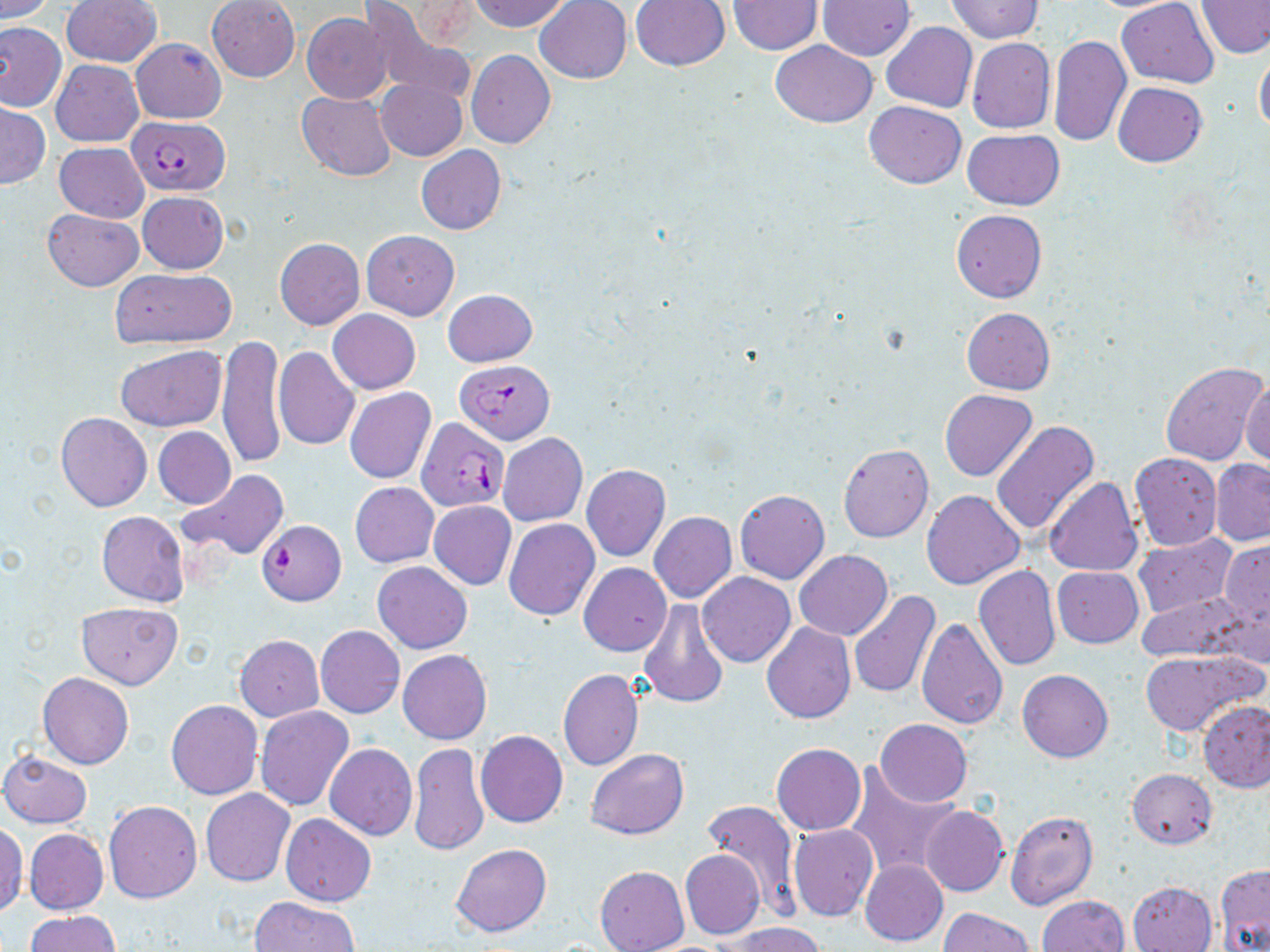 Approximate bounding boxes as [x1, y1, x2, y2] in pixels. Uninfected red blood cell locations: [1, 0, 55, 22], [61, 0, 161, 67], [356, 0, 475, 105], [470, 0, 571, 33], [534, 0, 632, 84], [728, 0, 823, 54], [818, 0, 914, 60], [949, 0, 1042, 42], [1117, 0, 1220, 87], [1197, 0, 1270, 59], [207, 1, 299, 82], [629, 1, 731, 72], [302, 14, 390, 103], [0, 21, 66, 112], [880, 22, 978, 113], [1047, 33, 1131, 147], [132, 37, 225, 123], [966, 37, 1056, 134], [769, 40, 877, 127], [1254, 46, 1270, 139], [466, 50, 556, 149], [52, 59, 144, 147], [376, 78, 468, 162], [1113, 82, 1207, 166], [297, 91, 395, 181], [864, 101, 967, 188], [1, 103, 50, 188], [961, 129, 1065, 210], [54, 141, 148, 222], [416, 145, 506, 235], [137, 191, 228, 274], [42, 209, 143, 291], [951, 209, 1047, 302], [362, 230, 459, 320], [275, 238, 365, 329], [109, 268, 236, 349], [443, 289, 537, 367], [962, 307, 1055, 394], [328, 309, 421, 394], [218, 335, 285, 469], [115, 344, 225, 432], [272, 346, 360, 451], [1160, 362, 1269, 467], [1242, 373, 1270, 470], [345, 387, 436, 483], [940, 389, 1037, 482], [55, 412, 152, 512], [990, 420, 1100, 536], [153, 426, 235, 509], [498, 433, 587, 527], [837, 444, 933, 543], [1129, 453, 1222, 551], [1210, 458, 1270, 545], [582, 464, 670, 561], [177, 469, 287, 561], [1043, 478, 1143, 577], [350, 482, 438, 567], [735, 490, 829, 584], [921, 490, 1025, 589], [428, 500, 516, 590], [97, 511, 189, 606], [649, 512, 737, 603], [504, 518, 598, 620], [1133, 532, 1237, 618], [1219, 540, 1269, 627], [794, 550, 893, 640], [373, 562, 472, 653], [579, 563, 671, 656], [973, 565, 1062, 670], [1052, 566, 1143, 647], [698, 572, 795, 667], [847, 590, 941, 700], [1136, 591, 1256, 663], [638, 600, 728, 710], [76, 601, 183, 689], [763, 603, 938, 709], [916, 617, 1007, 730], [761, 622, 856, 723], [315, 625, 404, 717], [235, 635, 323, 721], [397, 649, 492, 744], [1138, 650, 1261, 737], [557, 668, 643, 770], [1017, 669, 1112, 762], [38, 672, 133, 769], [166, 700, 263, 800], [1199, 700, 1270, 792], [256, 706, 353, 811], [874, 719, 971, 807], [476, 730, 568, 827], [324, 743, 417, 840], [409, 743, 488, 856], [771, 743, 866, 835], [585, 749, 689, 839], [1, 751, 91, 827], [848, 768, 961, 881], [1128, 768, 1216, 849], [201, 789, 295, 887], [104, 800, 202, 903], [701, 801, 802, 914], [920, 806, 1008, 897], [1004, 808, 1098, 911], [280, 814, 376, 907], [0, 822, 26, 917], [789, 824, 878, 921], [24, 829, 108, 914], [452, 844, 551, 937], [680, 850, 765, 939], [860, 859, 947, 947], [1215, 865, 1270, 951], [595, 866, 688, 952], [1126, 880, 1217, 952], [1037, 895, 1129, 952], [250, 897, 360, 952], [940, 909, 1033, 952], [25, 910, 122, 952], [726, 923, 823, 952]. Plasmodium falciparum-infected red blood cell locations: [127, 115, 230, 196], [455, 358, 557, 442], [417, 416, 507, 512], [257, 519, 345, 606]. Slide-level diagnosis: Plasmodium falciparum. Thin blood smear. May-Grünwald-Giemsa stain. 1000x magnification. Optical microscopy. Single field of view. Image is 1270×952 pixels.